Assess this cell for malaria.
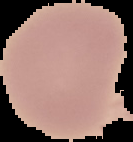

It is uninfected.

From a thin blood smear. The area outside the segmented cell region is set to black. Image is 133×142 pixels.